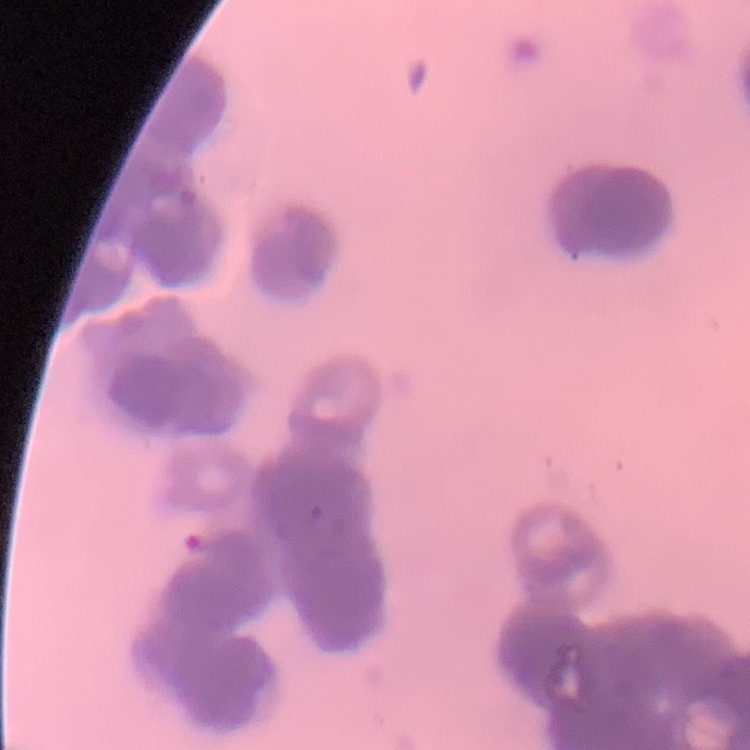

Summary:
  - Erythrocyte morphology: rouleaux formation
  - Preparation: thin peripheral smear
  - Stain: Field's or Giemsa
  - Image type: square crop of a larger photomicrograph